Comment on the morphology of the erythrocytes.
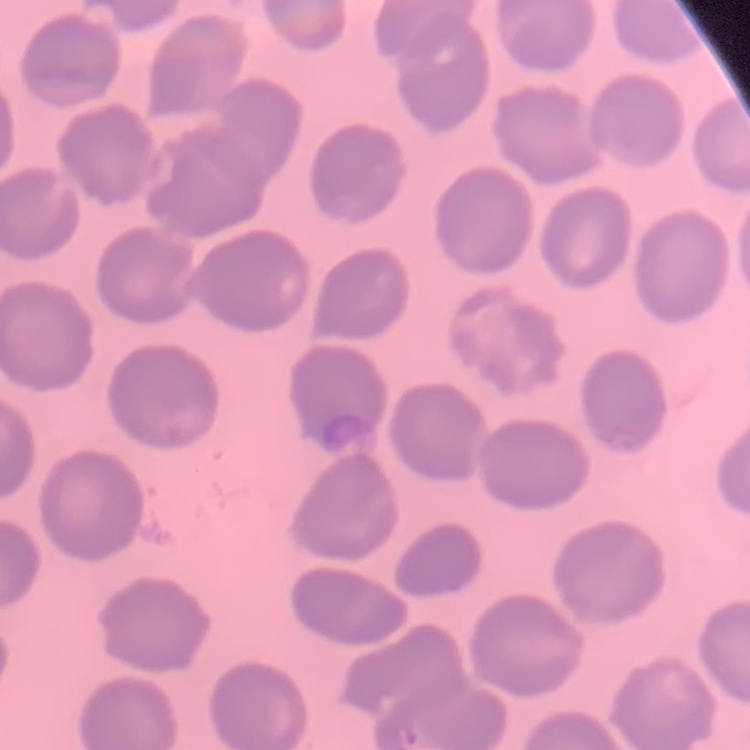

They show no rouleaux formation.

Summary:
  - Image type: one tile cut from a larger photomicrograph
  - Stain: Field's or Giemsa
  - Preparation: thin peripheral smear